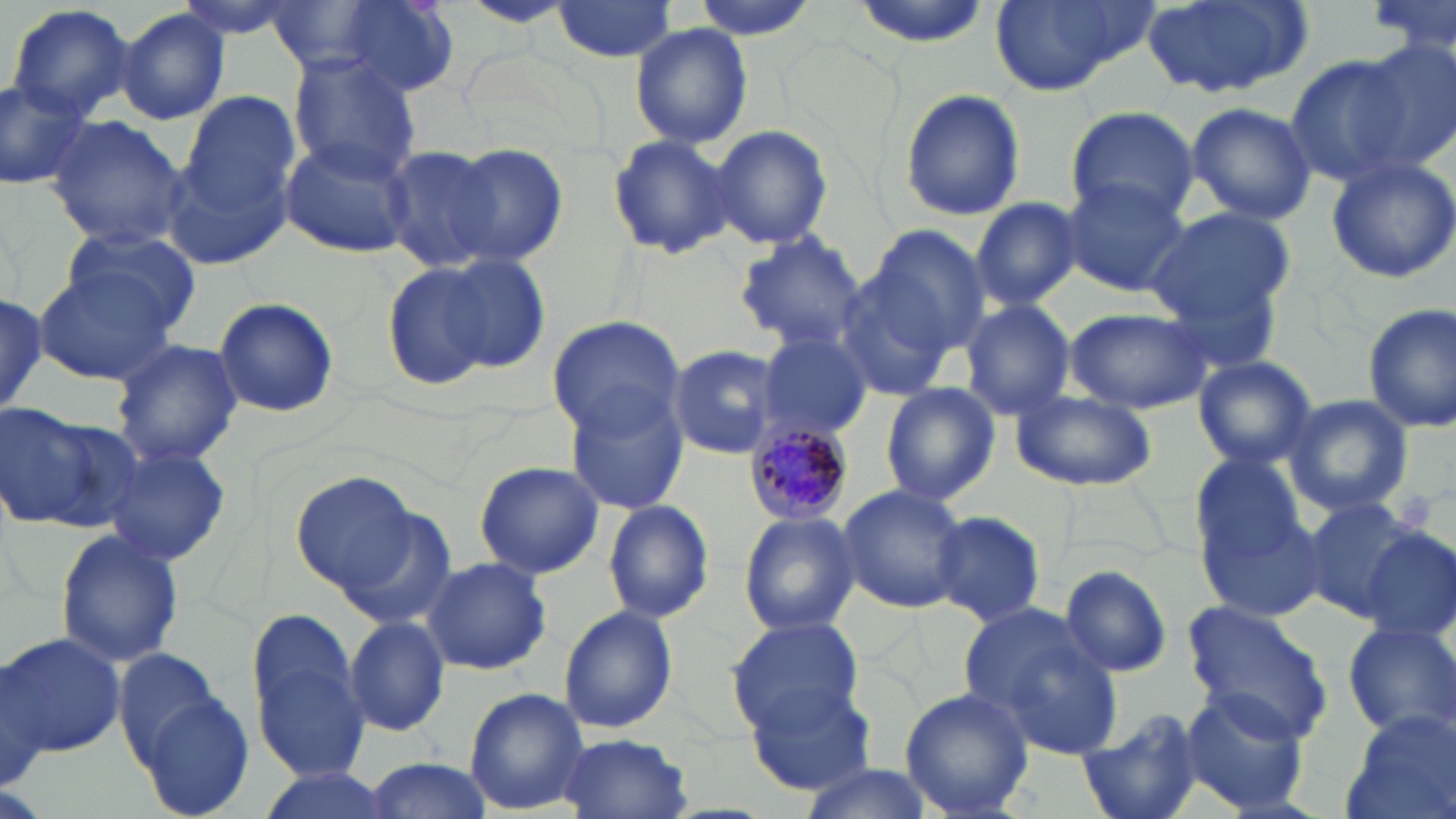
Summary:
  - Coordinate format: approximate bounding boxes as named x1/y1/x2/y2 corners in pixels
  - Plasmodium malariae-infected red blood cell locations: (x1=744, y1=421, x2=852, y2=526)
  - Uninfected red blood cell locations: (x1=169, y1=0, x2=309, y2=43), (x1=688, y1=0, x2=820, y2=39), (x1=847, y1=0, x2=996, y2=46), (x1=990, y1=0, x2=1154, y2=95), (x1=1144, y1=0, x2=1312, y2=100), (x1=1369, y1=0, x2=1455, y2=63), (x1=548, y1=1, x2=681, y2=63), (x1=265, y1=2, x2=384, y2=74), (x1=336, y1=2, x2=460, y2=99), (x1=458, y1=2, x2=575, y2=30), (x1=5, y1=3, x2=136, y2=121), (x1=116, y1=8, x2=229, y2=125), (x1=629, y1=23, x2=753, y2=150), (x1=1354, y1=38, x2=1456, y2=169), (x1=289, y1=54, x2=419, y2=178), (x1=1284, y1=55, x2=1409, y2=189), (x1=0, y1=75, x2=91, y2=191), (x1=175, y1=89, x2=304, y2=251), (x1=898, y1=89, x2=1025, y2=221), (x1=1184, y1=102, x2=1318, y2=226), (x1=1064, y1=106, x2=1201, y2=224), (x1=44, y1=116, x2=191, y2=247), (x1=710, y1=125, x2=833, y2=250), (x1=608, y1=135, x2=739, y2=259), (x1=278, y1=136, x2=415, y2=259), (x1=439, y1=142, x2=569, y2=266), (x1=381, y1=145, x2=506, y2=274), (x1=1323, y1=155, x2=1456, y2=284), (x1=1060, y1=176, x2=1192, y2=295), (x1=971, y1=197, x2=1081, y2=311), (x1=1149, y1=209, x2=1298, y2=330), (x1=862, y1=223, x2=990, y2=364), (x1=56, y1=224, x2=201, y2=341), (x1=735, y1=231, x2=868, y2=353), (x1=382, y1=254, x2=532, y2=393), (x1=835, y1=259, x2=972, y2=401), (x1=34, y1=266, x2=177, y2=384), (x1=213, y1=296, x2=340, y2=420), (x1=957, y1=297, x2=1078, y2=420), (x1=1362, y1=303, x2=1456, y2=432), (x1=1063, y1=305, x2=1215, y2=414), (x1=546, y1=316, x2=687, y2=439), (x1=756, y1=331, x2=873, y2=440), (x1=109, y1=337, x2=242, y2=466), (x1=666, y1=344, x2=784, y2=459), (x1=1191, y1=356, x2=1318, y2=470), (x1=880, y1=383, x2=999, y2=507), (x1=566, y1=388, x2=691, y2=513), (x1=1006, y1=389, x2=1159, y2=491), (x1=1281, y1=395, x2=1414, y2=516), (x1=1, y1=400, x2=138, y2=537), (x1=102, y1=446, x2=232, y2=568), (x1=473, y1=461, x2=604, y2=580), (x1=1194, y1=467, x2=1321, y2=618), (x1=291, y1=472, x2=421, y2=597), (x1=836, y1=483, x2=968, y2=614), (x1=1302, y1=497, x2=1426, y2=621), (x1=603, y1=498, x2=715, y2=625), (x1=334, y1=503, x2=460, y2=630), (x1=931, y1=510, x2=1047, y2=628), (x1=737, y1=511, x2=862, y2=636), (x1=54, y1=528, x2=184, y2=669), (x1=1359, y1=529, x2=1456, y2=639), (x1=421, y1=556, x2=551, y2=677), (x1=1061, y1=564, x2=1173, y2=677), (x1=1180, y1=603, x2=1333, y2=741), (x1=558, y1=605, x2=678, y2=733), (x1=961, y1=607, x2=1123, y2=761), (x1=249, y1=610, x2=369, y2=778), (x1=344, y1=615, x2=450, y2=738), (x1=726, y1=617, x2=869, y2=737), (x1=1341, y1=618, x2=1456, y2=741), (x1=4, y1=630, x2=125, y2=761), (x1=114, y1=649, x2=231, y2=770), (x1=0, y1=655, x2=55, y2=794), (x1=743, y1=681, x2=878, y2=796), (x1=1179, y1=686, x2=1311, y2=815), (x1=464, y1=688, x2=590, y2=814), (x1=900, y1=688, x2=1034, y2=818), (x1=135, y1=692, x2=257, y2=819), (x1=1340, y1=706, x2=1455, y2=819), (x1=1075, y1=709, x2=1208, y2=819), (x1=559, y1=734, x2=692, y2=818), (x1=360, y1=757, x2=495, y2=819), (x1=795, y1=762, x2=936, y2=819), (x1=248, y1=767, x2=395, y2=819)
  - Slide-level diagnosis: Plasmodium malariae
  - Field of view: single
  - Stain: May-Grünwald-Giemsa
  - Image size: 1456×819 pixels
  - Magnification: 1000x
  - Preparation: thin blood film
  - Modality: optical microscopy